Give the position of every Plasmodium parasite visible.
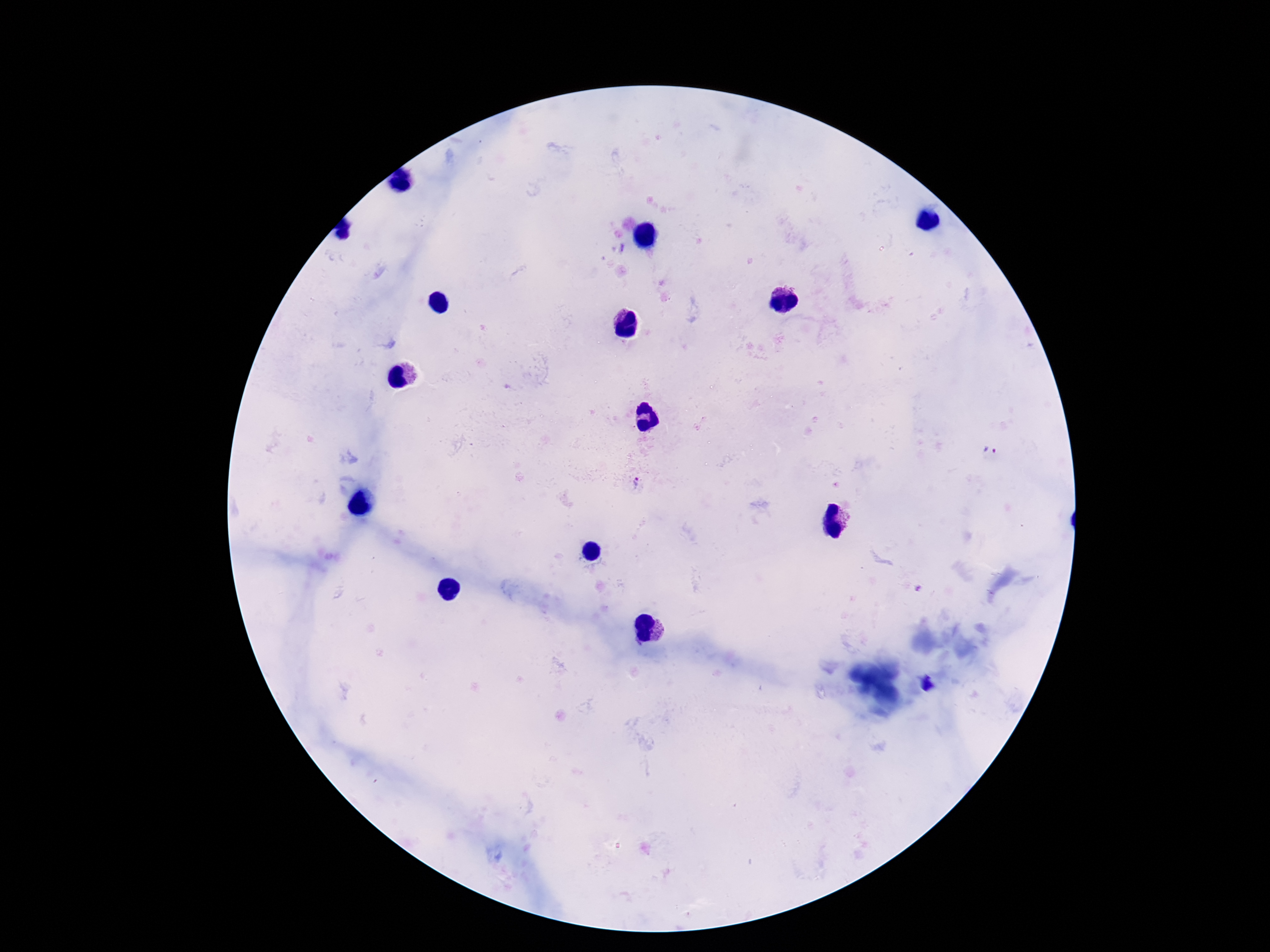

Approximate centers as (x, y) in pixels.
Plasmodium parasites: (990, 449), (636, 484).

Image is 1270×952 pixels. Giemsa-stained preparation. Patient malaria status: infected. Smartphone photograph taken through the microscope eyepiece. Thick blood smear. 100x magnification. Single field of view.